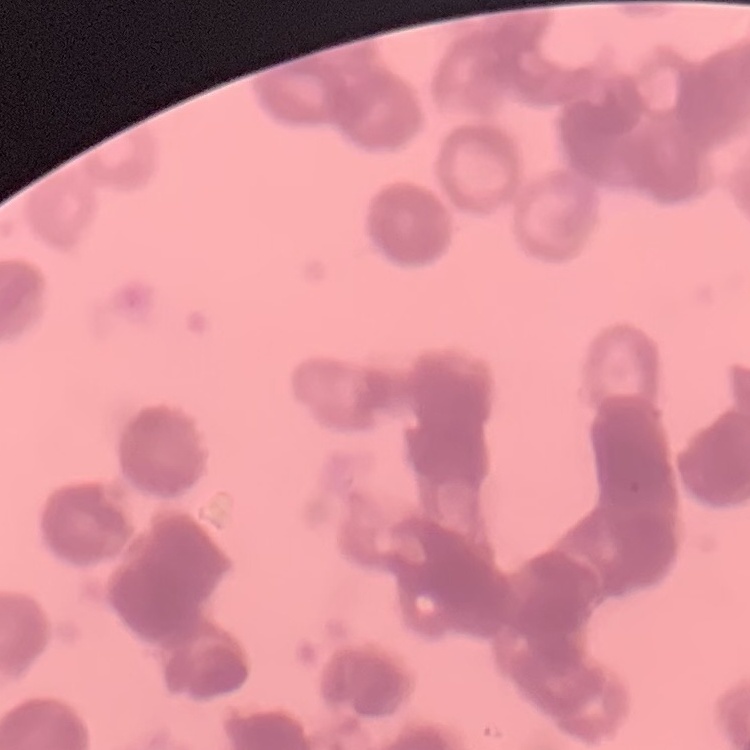

{
  "red_blood_cell_morphology": "rouleaux formation",
  "preparation": "thin blood film",
  "image_type": "one tile cut from a larger photomicrograph",
  "stain": "Field's or Giemsa"
}